Assess the background quality.
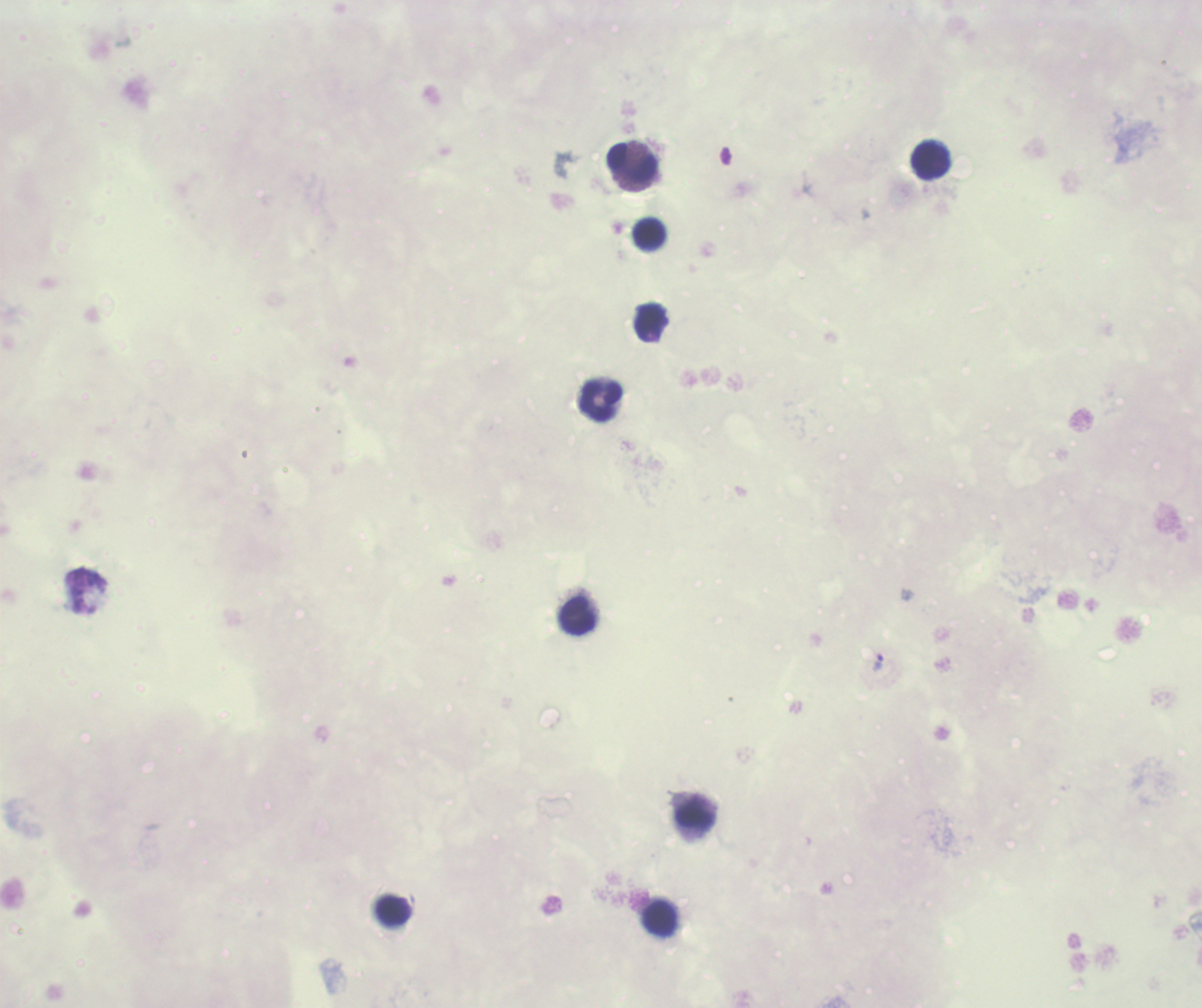

Poor.

coordinate format = approximate centers as [x, y] in pixels
leukocyte locations = [931, 161], [632, 163], [649, 234], [601, 400], [578, 616], [695, 816], [394, 911], [660, 919]
trophozoite locations = [878, 662]
stain = Romanowsky
image size = 1202×1008 pixels
preparation = thick smear of blood
result = malaria parasites identified
field of view = one from this slide
coloration quality = bad
magnification = 100x
context = previously used in a real diagnosis